Locate every malaria parasite by life-cycle stage, and every leukocyte.
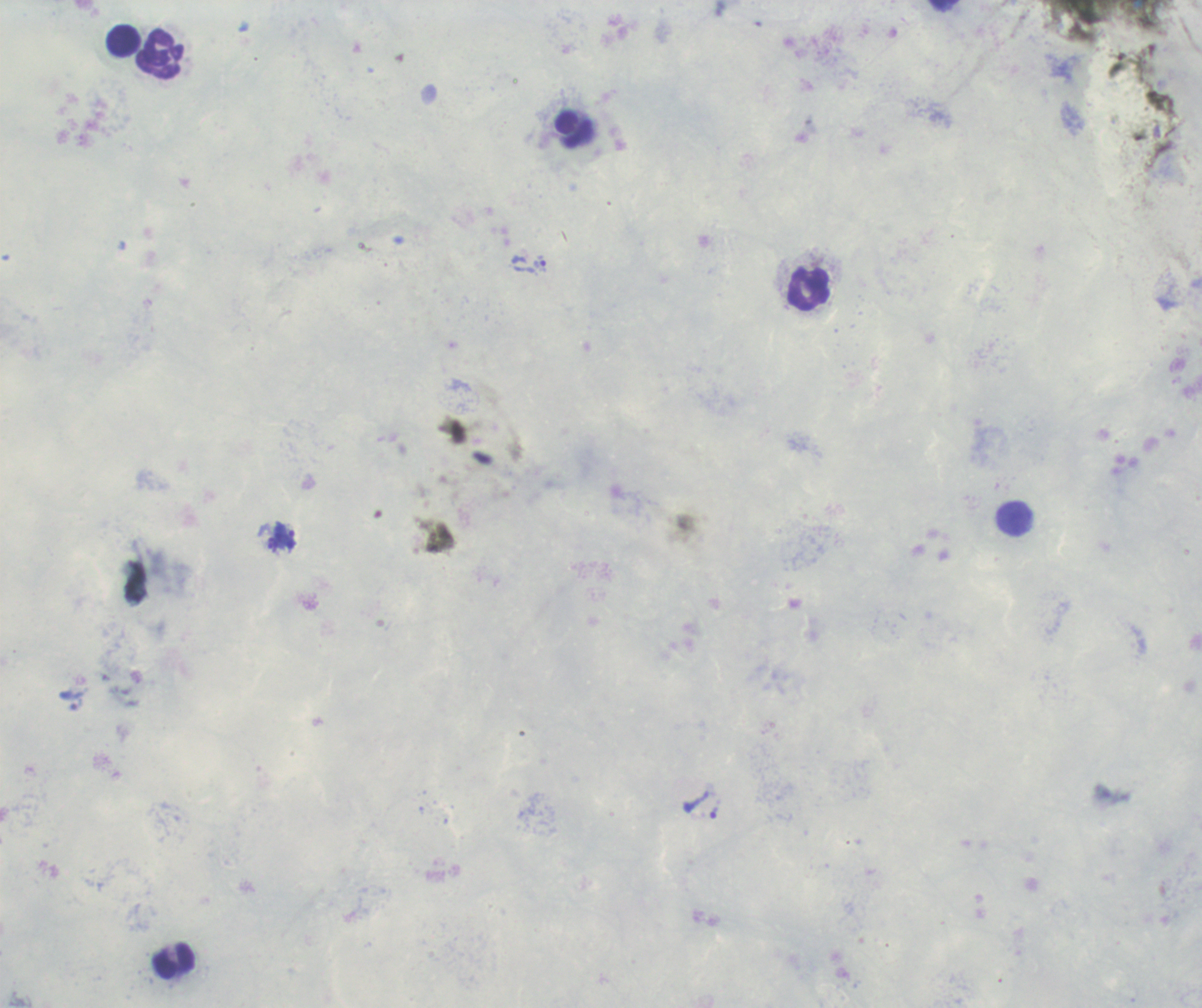

Approximate centers as (x, y) in pixels.
Trophozoites: (541, 264), (286, 535), (272, 544).
No schizont or gametocyte forms observed.
Leukocytes: (123, 40), (160, 55), (574, 130), (807, 289), (1015, 520), (174, 963).

Summary:
  - Background quality: poor
  - Preparation: thick blood smear
  - Context: previously used in an actual diagnosis
  - Magnification: 100x
  - Image size: 1202×1008 pixels
  - Field of view: one from this slide
  - Coloration quality: good
  - Stain: Romanowsky